Report the malaria status of this cell.
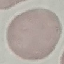
It is uninfected.

preparation = thin smear
image type = automatically extracted cell patch, resized to 64 × 64 pixels
stain = Giemsa
capture = smartphone through the microscope eyepiece